Name the cell type shown.
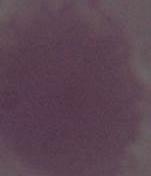
This is an erythrocyte.

Micrograph. Captured at 1000x magnification.